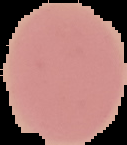 The area outside the segmented cell region is set to black. Result: no Plasmodium parasites detected. Image is 127×145 pixels. From a thin blood film.